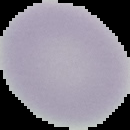
malaria_status: uninfected
image_size: 130×130 pixels
image_type: segmented cell region on a black background
preparation: thin blood film